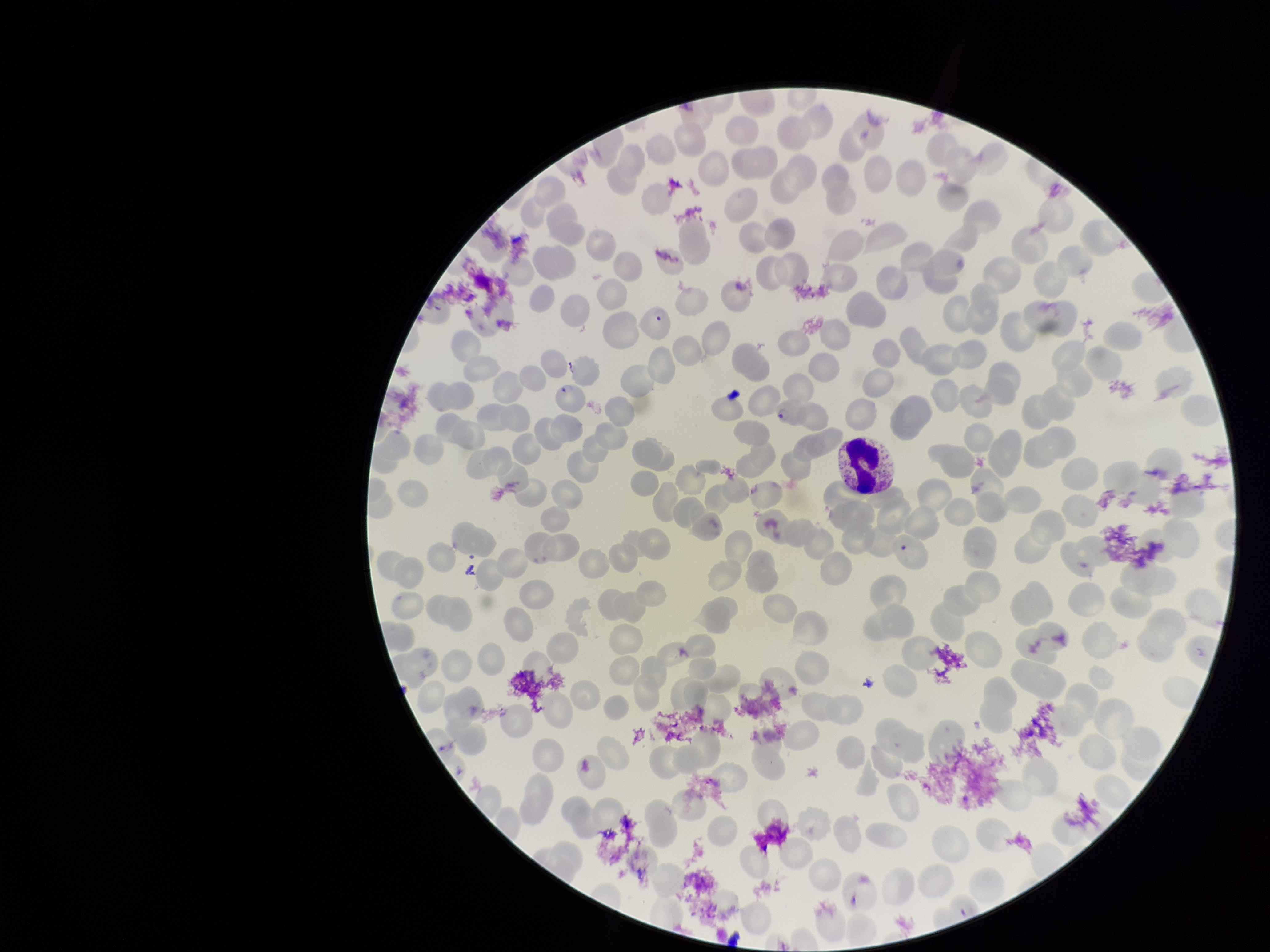 Stained with Giemsa. Parasitized red blood cell count: 3. Preparation: thin smear. Smartphone photograph taken through the eyepiece of a microscope. Red blood cell count: 265. Patient malaria status: positive. Species reported for this patient: Plasmodium falciparum. Image is 1270×952 pixels. One field from this slide. Parasitized red blood cells: detected.